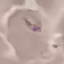 Malaria status: parasitized. Giemsa-stained preparation. Photographed with a smartphone camera at the microscope eyepiece. Thin blood smear. Automatically extracted cell patch, resized to 64 × 64 pixels.